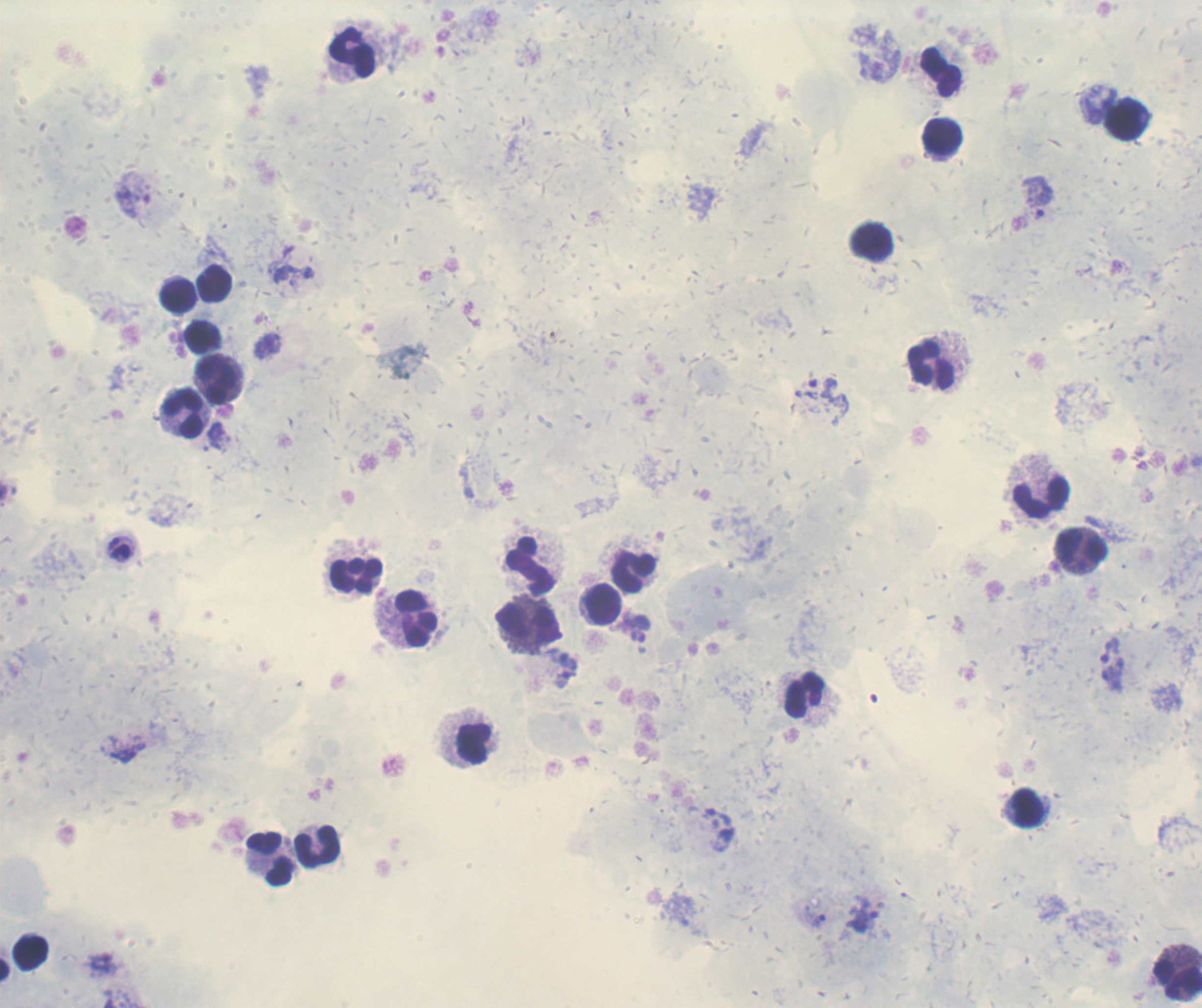
Approximate centers as [x, y] in pixels. Trophozoite locations: [879, 65], [1037, 190], [133, 194], [1038, 214], [293, 270], [267, 345], [819, 397], [217, 436], [121, 542], [637, 636], [564, 661], [1111, 662], [565, 679], [126, 753], [719, 828], [862, 916], [814, 919], [101, 964]. Leukocyte locations: [351, 51], [940, 71], [1127, 120], [942, 139], [871, 242], [216, 283], [176, 295], [201, 335], [931, 365], [218, 379], [184, 412], [1042, 497], [1081, 547], [530, 567], [634, 574], [356, 575], [604, 605], [417, 619], [528, 626], [805, 696], [473, 742], [1026, 809], [317, 847], [270, 858], [31, 952], [1175, 977]. Image is 1202×1008 pixels. Romanowsky-stained preparation. Result: malaria parasites identified. Background quality: good. One field from this slide. Captured at 100x magnification. Coloration quality: good. Thick blood smear. Previously used in an actual diagnosis.